Report the malaria status of this cell.
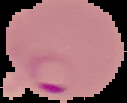

It is parasitized.

Image is 127×103 pixels. The area outside the segmented cell region is set to black. From a thin blood smear.